Give the position of every leukocyte visible.
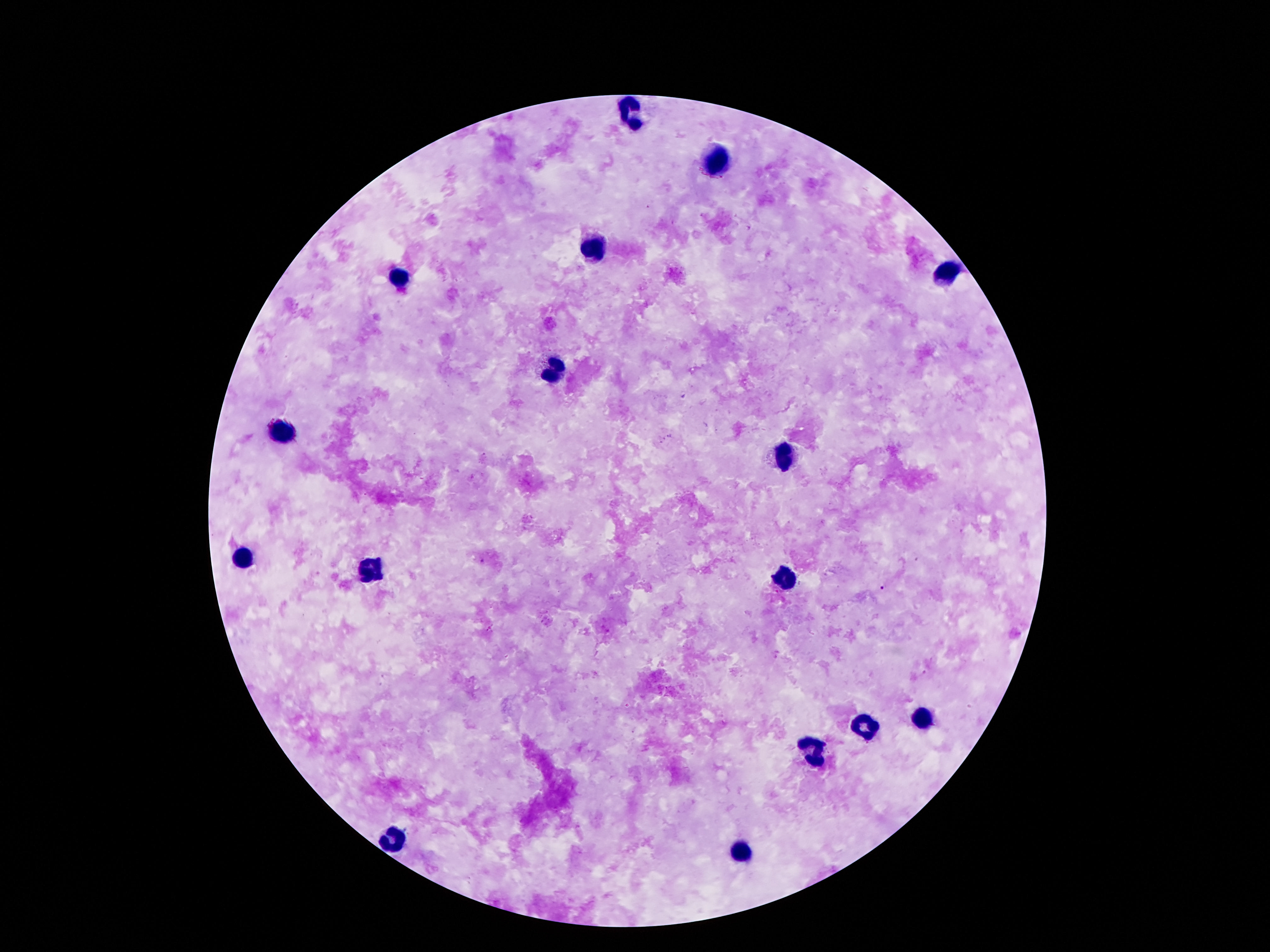
Approximate object centers, in pixels from the top-left corner.
Leukocytes: (x=628, y=112), (x=716, y=158), (x=590, y=248), (x=945, y=276), (x=399, y=279), (x=552, y=372), (x=279, y=431), (x=781, y=458), (x=239, y=559), (x=369, y=572), (x=783, y=576), (x=923, y=718), (x=863, y=724), (x=812, y=755), (x=393, y=840), (x=741, y=856).

Thick peripheral-blood smear. One field from this slide. 100x magnification. Smartphone photograph taken through the microscope eyepiece. Giemsa-stained preparation. Patient malaria status: not infected. Image is 1270×952 pixels.